Locate and identify every blood parasite.
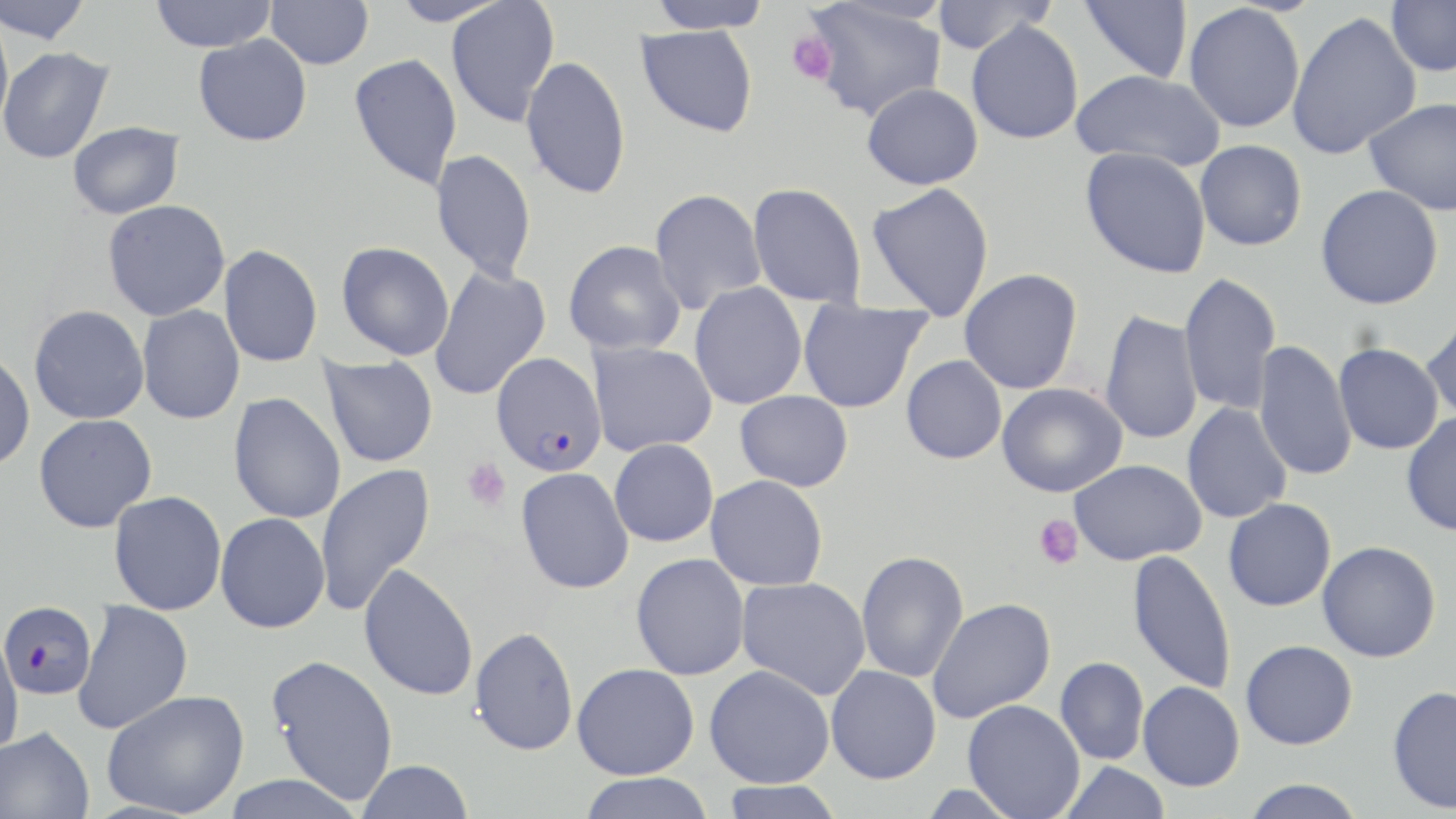

Approximate bounding boxes as [x1, y1, x2, y2] in pixels.
Plasmodium falciparum-infected red blood cells: [491, 352, 608, 477], [0, 600, 96, 701].
No Plasmodium ovale, Plasmodium malariae, Plasmodium vivax, Babesia divergens, or Trypanosoma brucei observed.

slide-level diagnosis = Plasmodium falciparum
magnification = 1000x
preparation = thin blood smear
platelet locations = approximate bounding boxes as [x1, y1, x2, y2] in pixels: [785, 31, 837, 86], [461, 457, 511, 512], [1034, 515, 1083, 570]
stain = May-Grünwald-Giemsa
image size = 1456×819 pixels
modality = optical microscopy
uninfected red blood cell locations = approximate bounding boxes as [x1, y1, x2, y2] in pixels: [0, 0, 93, 46], [150, 0, 277, 53], [266, 0, 374, 69], [388, 0, 511, 26], [646, 0, 773, 33], [801, 0, 947, 121], [930, 0, 1055, 54], [1080, 0, 1193, 83], [1386, 0, 1456, 76], [446, 1, 560, 127], [1183, 3, 1305, 133], [1286, 10, 1422, 161], [0, 11, 14, 139], [966, 20, 1084, 144], [636, 24, 758, 138], [194, 34, 312, 146], [0, 46, 115, 164], [348, 53, 463, 191], [521, 55, 632, 200], [1071, 69, 1225, 173], [861, 83, 984, 190], [1365, 97, 1456, 216], [67, 121, 185, 219], [1195, 140, 1307, 251], [1080, 146, 1212, 278], [430, 149, 537, 283], [747, 182, 866, 306], [867, 182, 995, 320], [1315, 184, 1443, 309], [649, 189, 766, 315], [102, 199, 231, 321], [564, 240, 686, 356], [336, 241, 454, 360], [219, 244, 323, 367], [429, 263, 551, 402], [959, 268, 1083, 394], [1178, 271, 1281, 414], [689, 282, 807, 410], [798, 299, 932, 413], [29, 304, 149, 424], [137, 305, 245, 424], [1420, 308, 1456, 421], [1099, 310, 1203, 447], [1253, 340, 1356, 483], [587, 341, 717, 457], [1333, 343, 1444, 455], [0, 351, 36, 472], [320, 355, 439, 468], [901, 355, 1007, 464], [997, 382, 1127, 497], [734, 390, 853, 491], [229, 392, 346, 525], [1181, 402, 1292, 524], [1401, 412, 1456, 536], [34, 414, 157, 533], [609, 439, 719, 547], [1069, 459, 1206, 565], [314, 463, 436, 617], [516, 467, 635, 595], [706, 475, 829, 591], [109, 491, 227, 616], [1223, 498, 1337, 612], [215, 513, 330, 633], [1317, 540, 1441, 662], [1127, 549, 1236, 695], [856, 550, 969, 682], [631, 552, 750, 680], [359, 564, 479, 701], [736, 576, 871, 700], [927, 597, 1055, 723], [73, 600, 193, 735], [469, 626, 579, 756], [0, 629, 23, 759], [1240, 639, 1358, 749], [266, 654, 399, 805], [1055, 657, 1149, 765], [572, 662, 699, 779], [705, 664, 835, 788], [826, 665, 941, 784], [1138, 681, 1245, 791], [1387, 685, 1456, 814], [102, 689, 250, 818], [962, 699, 1085, 819], [0, 725, 95, 819], [358, 759, 473, 819], [1059, 761, 1170, 819], [577, 773, 716, 819], [220, 774, 368, 819], [1241, 779, 1366, 818], [716, 780, 846, 819]
field of view = single